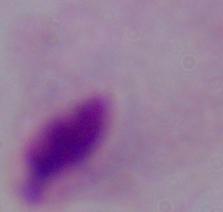
Photomicrograph. A trichomonad is seen. 1000x magnification.